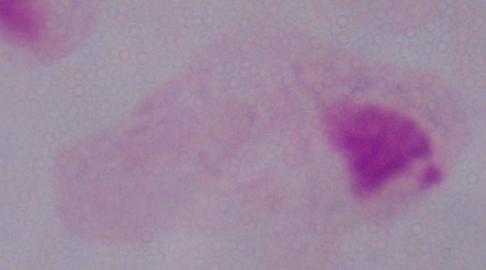
Summary:
  - Modality: photomicrograph
  - Identification: trichomonad
  - Magnification: 1000x